Classify this cell by malaria status.
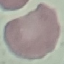
It is uninfected.

{
  "preparation": "thin smear",
  "capture": "smartphone through the microscope eyepiece",
  "stain": "Giemsa",
  "image_type": "automatically extracted cell patch, resized to 64 × 64 pixels"
}